Name the blood parasite species.
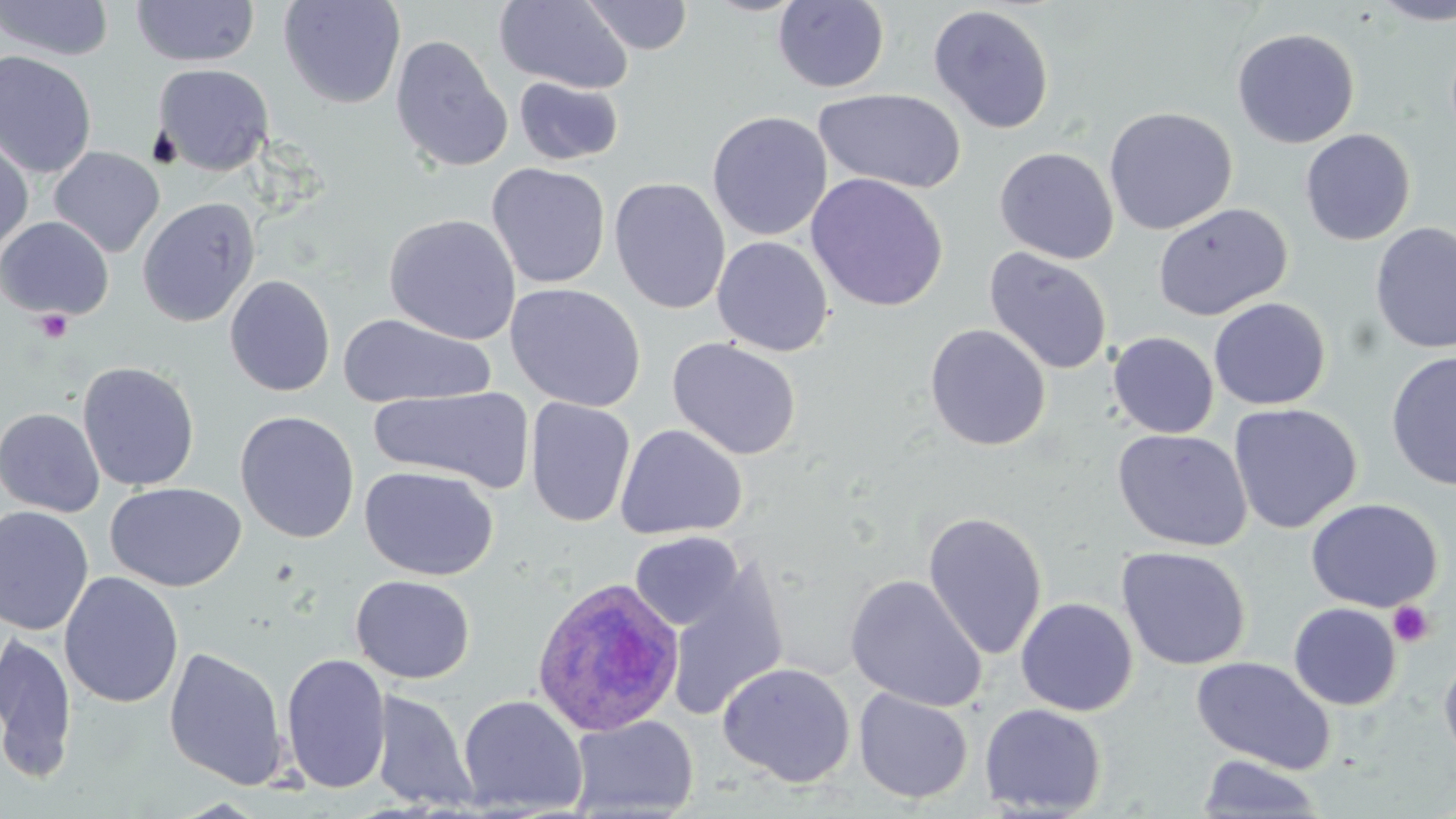
Plasmodium ovale.

stain = May-Grünwald-Giemsa
field of view = one of a larger specimen
image size = 1456×819 pixels
preparation = thin blood smear
uninfected red blood cell locations = approximate bounding boxes as (x1, y1, x2, y2) in pixels: (130, 0, 260, 68), (278, 0, 406, 110), (494, 0, 634, 94), (581, 0, 694, 55), (1371, 0, 1456, 25), (0, 1, 115, 62), (772, 1, 890, 93), (928, 4, 1055, 134), (1231, 27, 1360, 148), (390, 34, 513, 173), (0, 50, 97, 178), (152, 63, 274, 176), (513, 76, 624, 166), (812, 87, 966, 194), (1103, 106, 1238, 235), (706, 110, 833, 241), (1299, 128, 1416, 246), (0, 135, 34, 257), (48, 146, 165, 257), (994, 146, 1119, 265), (487, 162, 611, 289), (805, 172, 948, 312), (609, 177, 730, 314), (136, 197, 260, 327), (1152, 202, 1292, 322), (383, 213, 521, 345), (0, 216, 114, 321), (1370, 221, 1456, 355), (712, 235, 834, 357), (984, 247, 1112, 376), (224, 274, 336, 397), (505, 283, 647, 412), (1208, 297, 1331, 410), (339, 313, 496, 408), (924, 323, 1051, 451), (1108, 331, 1219, 438), (666, 337, 802, 460), (1385, 350, 1456, 491), (78, 361, 199, 492), (369, 386, 533, 493), (525, 397, 636, 528), (1228, 403, 1362, 534), (0, 407, 105, 517), (234, 411, 360, 543), (615, 424, 748, 540), (1112, 428, 1253, 552), (360, 465, 499, 580), (105, 482, 247, 592), (1306, 497, 1443, 613), (0, 505, 95, 635), (922, 510, 1048, 661), (630, 531, 743, 631), (1116, 546, 1251, 670), (664, 557, 790, 722), (60, 572, 184, 709), (845, 574, 986, 711), (350, 575, 476, 684), (1015, 597, 1138, 716), (1288, 602, 1401, 710), (0, 630, 78, 783), (163, 646, 289, 790), (1438, 649, 1456, 772), (280, 652, 392, 795), (1191, 656, 1336, 774), (717, 662, 855, 787), (854, 687, 974, 803), (370, 689, 477, 811), (457, 694, 588, 816), (854, 695, 1109, 807), (979, 703, 1107, 816), (567, 714, 699, 818), (1196, 754, 1328, 817)
Plasmodium ovale-infected red blood cell locations = approximate bounding boxes as (x1, y1, x2, y2) in pixels: (530, 577, 686, 737)
modality = optical microscopy
platelet locations = approximate bounding boxes as (x1, y1, x2, y2) in pixels: (34, 309, 73, 343), (1387, 601, 1435, 647)
magnification = 1000x